Name the parasite shown.
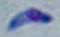

Toxoplasma gondii.

{
  "modality": "micrograph",
  "magnification": "1000x"
}